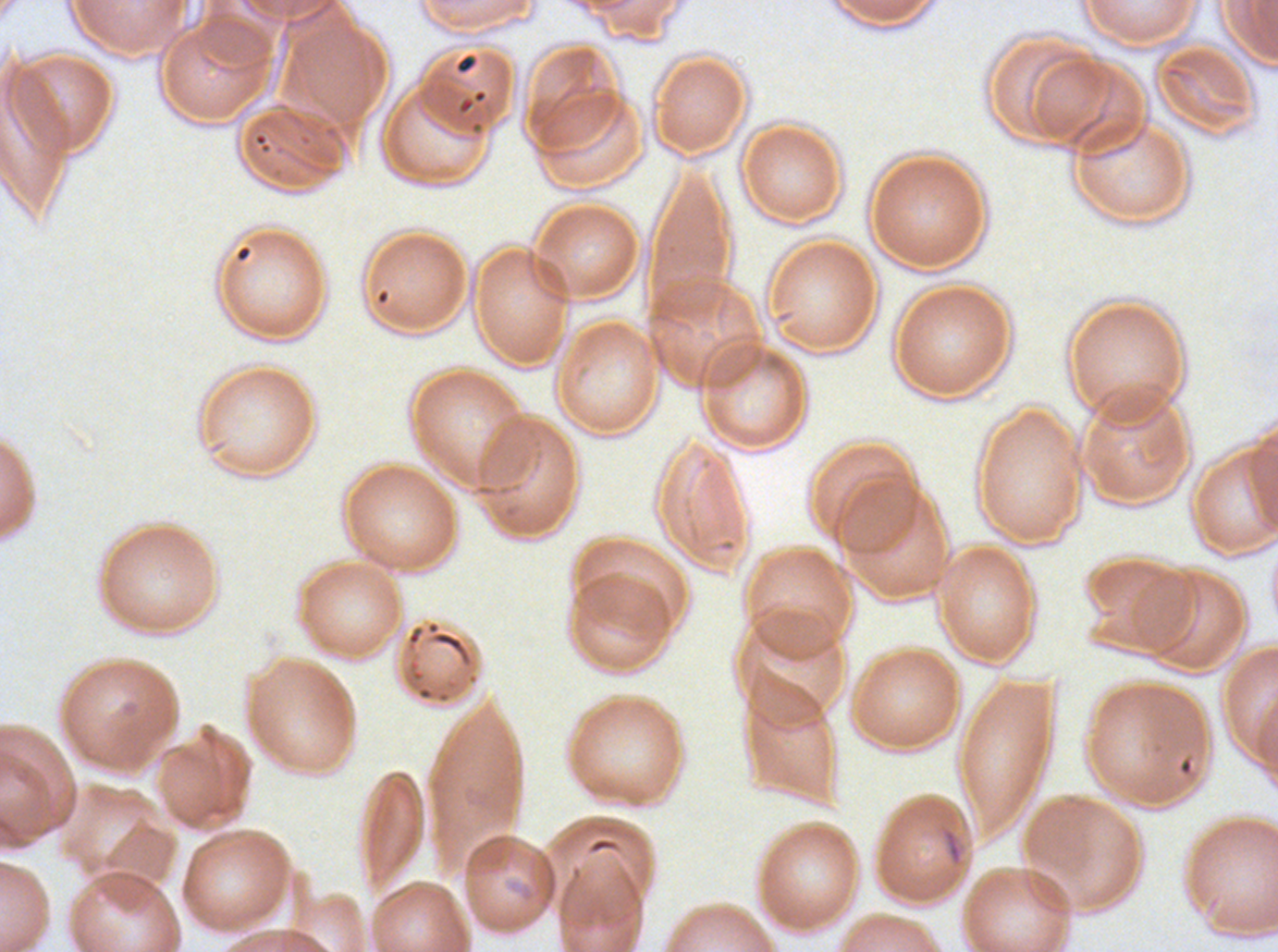

Approximate bounding boxes as {x1, y1, x2, y2} in pixels.
Summary:
  - Debris locations: {941, 827, 964, 867}
  - Preparation: thin blood smear
  - Image size: 1278×952 pixels
  - Stain: Giemsa
  - Specimen: Plasmodium falciparum from a patient in The Gambia, cultured ex vivo for 24 to 48 hours
  - Field of view: sub-image separated from a larger composite